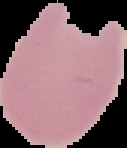
malaria status = parasitized
preparation = thin blood film
image type = segmented cell region on a black background
image size = 127×148 pixels